Identify the cell.
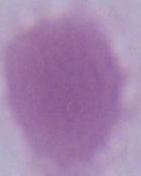
An erythrocyte.

modality: micrograph
magnification: 1000x